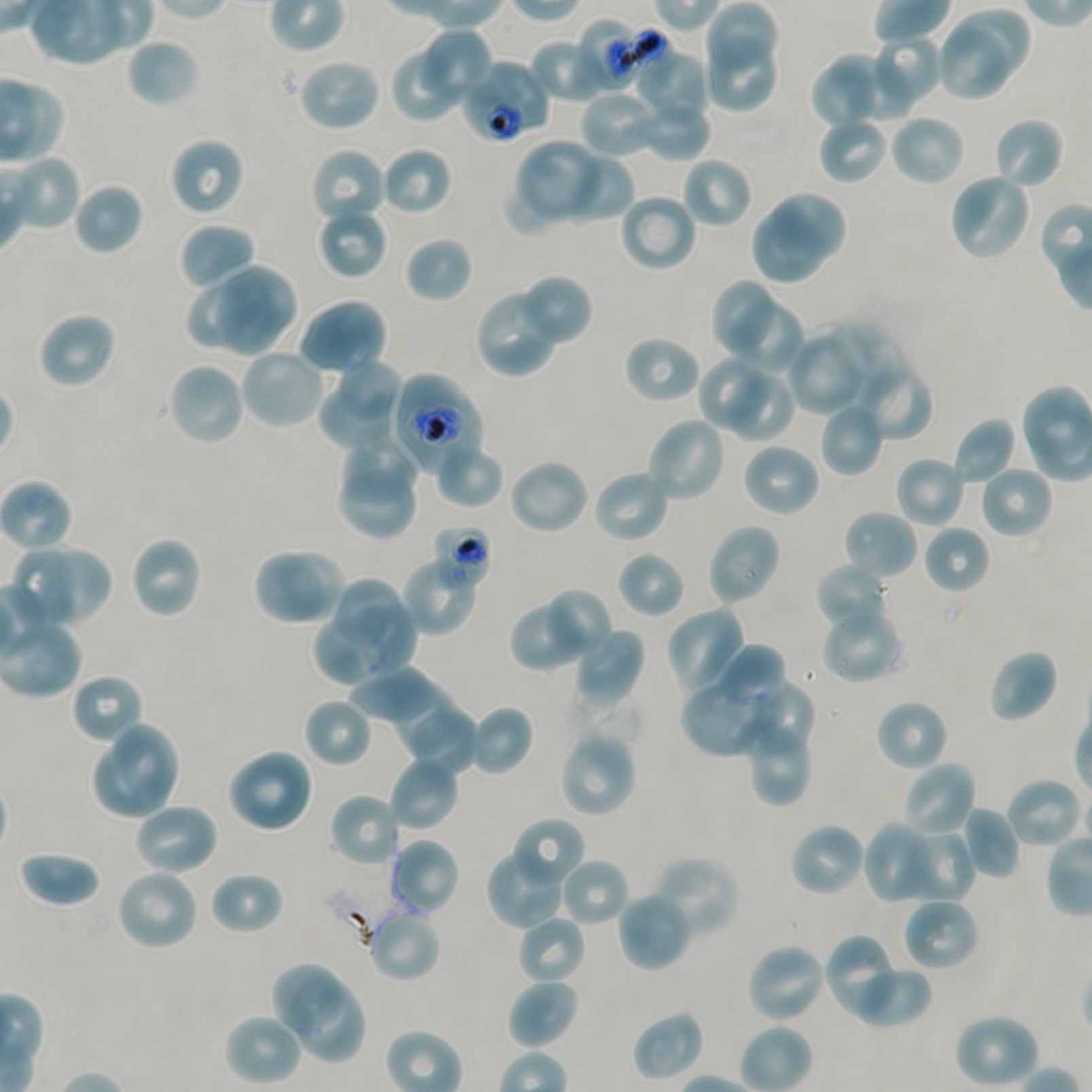
Approximate bounding boxes as {x1, y1, x2, y2} in pixels. Not every red blood cell is marked. A life-cycle stage — or a range of stages, where the recorded stages span more than one — follows each staged infected red blood cell. Locations of uninfected red blood cells: {706, 3, 778, 78}, {950, 7, 1031, 84}, {420, 27, 494, 101}, {937, 28, 1008, 101}, {869, 33, 943, 111}, {526, 36, 610, 104}, {126, 37, 200, 109}, {702, 44, 778, 113}, {389, 46, 469, 123}, {829, 51, 912, 124}, {637, 52, 709, 126}, {296, 56, 382, 133}, {809, 67, 875, 131}, {580, 90, 663, 158}, {633, 99, 710, 162}, {890, 114, 967, 187}, {818, 115, 888, 185}, {992, 117, 1065, 191}, {168, 136, 246, 217}, {514, 140, 602, 220}, {381, 146, 453, 216}, {309, 147, 387, 226}, {553, 152, 634, 225}, {680, 156, 752, 230}, {948, 172, 1032, 262}, {505, 176, 562, 232}, {73, 183, 143, 256}, {618, 192, 698, 274}, {771, 194, 848, 260}, {316, 205, 389, 280}, {750, 209, 828, 285}, {178, 223, 257, 293}, {403, 236, 473, 302}, {224, 263, 297, 337}, {216, 267, 278, 358}, {516, 274, 593, 346}, {714, 282, 771, 352}, {189, 283, 252, 348}, {474, 289, 560, 378}, {297, 297, 387, 376}, {731, 299, 802, 376}, {37, 312, 117, 390}, {818, 321, 903, 408}, {787, 331, 867, 416}, {623, 334, 702, 405}, {239, 347, 327, 430}, {697, 354, 765, 431}, {853, 359, 934, 442}, {167, 361, 247, 447}, {335, 362, 403, 416}, {726, 370, 797, 444}, {335, 378, 420, 490}, {318, 386, 399, 452}, {819, 401, 884, 477}, {645, 416, 728, 504}, {950, 416, 1019, 487}, {341, 433, 420, 504}, {435, 441, 505, 510}, {741, 441, 821, 518}, {894, 455, 967, 530}, {507, 457, 590, 536}, {979, 464, 1054, 539}, {338, 469, 414, 541}, {591, 469, 672, 545}, {843, 509, 919, 583}, {706, 522, 782, 606}, {923, 524, 990, 595}, {130, 534, 204, 619}, {44, 543, 113, 624}, {10, 549, 74, 629}, {616, 550, 685, 619}, {252, 553, 327, 627}, {283, 553, 344, 621}, {400, 554, 481, 636}, {814, 562, 890, 634}, {329, 576, 411, 649}, {538, 588, 613, 663}, {509, 600, 581, 673}, {346, 602, 416, 678}, {665, 605, 749, 697}, {314, 613, 386, 685}, {825, 616, 903, 684}, {571, 626, 645, 710}, {718, 647, 787, 711}, {987, 649, 1059, 723}, {347, 666, 442, 725}, {70, 673, 145, 746}, {680, 676, 776, 757}, {758, 680, 816, 752}, {392, 682, 459, 755}, {304, 698, 373, 768}, {875, 699, 949, 773}, {465, 705, 533, 776}, {408, 710, 479, 772}, {114, 721, 181, 805}, {750, 725, 807, 805}, {558, 730, 638, 818}, {94, 742, 164, 818}, {226, 747, 314, 834}, {388, 755, 460, 833}, {903, 761, 977, 839}, {1004, 777, 1084, 850}, {328, 791, 403, 867}, {132, 801, 219, 876}, {958, 805, 1021, 880}, {511, 817, 586, 888}, {860, 820, 938, 905}, {787, 821, 866, 898}, {900, 826, 976, 903}, {388, 837, 461, 917}, {486, 845, 569, 930}, {18, 849, 102, 907}, {651, 856, 740, 939}, {558, 857, 630, 928}, {115, 867, 200, 951}, {209, 871, 285, 936}, {616, 891, 694, 972}, {901, 896, 980, 972}, {366, 908, 442, 983}, {515, 914, 586, 985}, {823, 932, 898, 1019}, {745, 943, 826, 1024}, {852, 963, 932, 1030}, {272, 964, 347, 1034}, {506, 978, 580, 1050}, {293, 980, 367, 1065}, {632, 1010, 705, 1082}, {223, 1013, 304, 1086}, {953, 1013, 1041, 1089}. Locations of infected red blood cells: {391, 372, 484, 476} trophozoite. Locations of red blood cells of indeterminate infection status: {575, 17, 641, 88}, {627, 23, 678, 90}, {460, 59, 550, 145}, {431, 523, 492, 587}. Blood group of the donor: A+/O+. Image is 1092×1092 pixels. P. falciparum strain NF54 maintained in static in-vitro culture. Giemsa stain. Single field of view. Thin blood smear. 100x oil-immersion objective, numerical aperture 1.45.